Assess this cell for malaria.
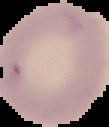
Uninfected.

From a thin blood film. Image is 109×127 pixels. Cell region segmented out of the field of view; the surrounding area is masked to black.